State the blood parasite species.
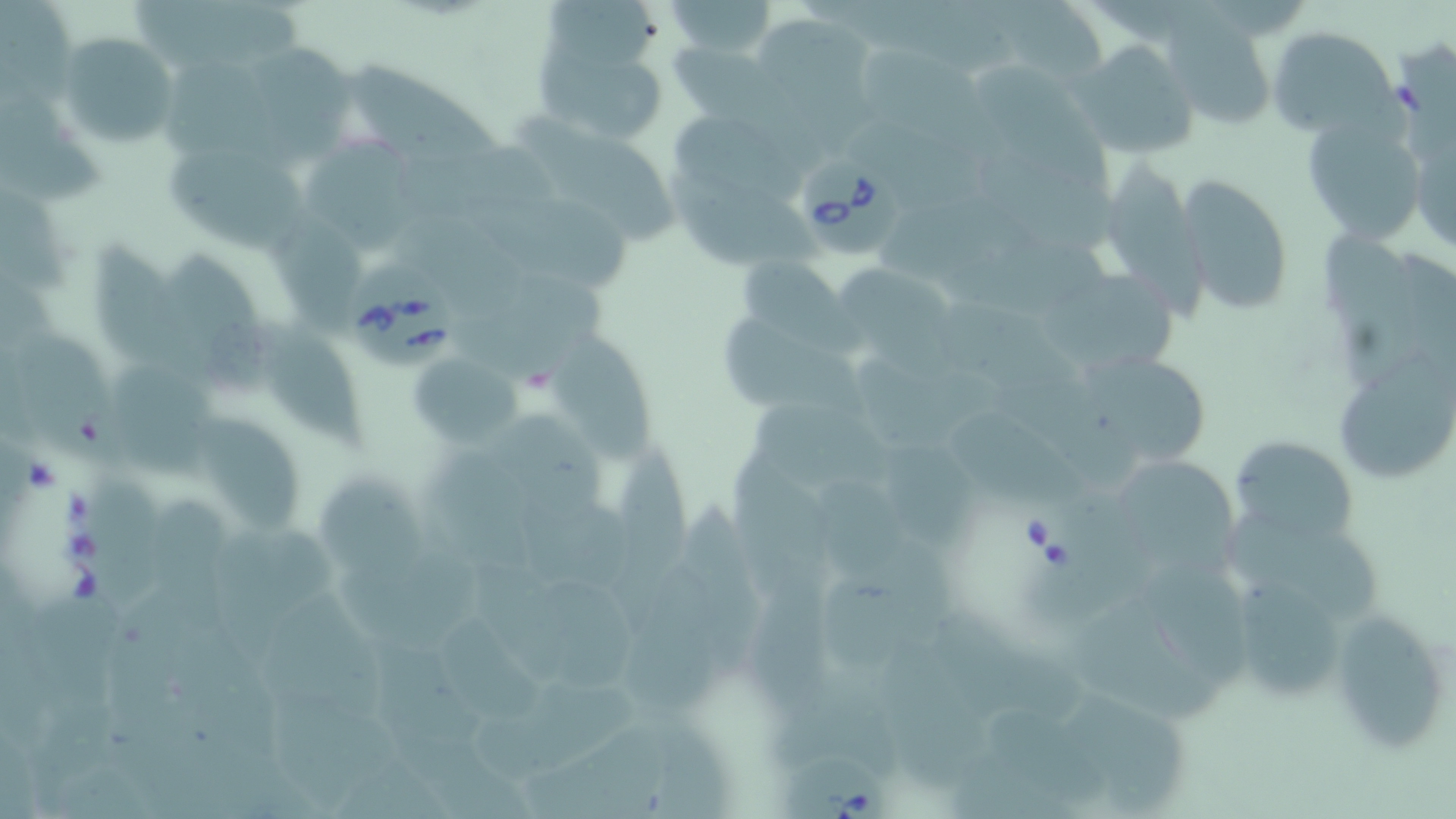

Babesia divergens.

Summary:
  - Coordinate format: approximate bounding boxes as (x1,y1)-(x2,y2) corner pairs in pixels
  - Babesia divergens-infected red blood cell locations: (794,152)-(906,262), (343,260)-(459,365), (1014,489)-(1144,628), (776,746)-(896,819)
  - Uninfected red blood cell locations: (2,0)-(79,103), (133,0)-(302,70), (545,0)-(653,71), (661,0)-(778,59), (1158,12)-(1280,128), (762,15)-(877,149), (1268,27)-(1398,137), (57,33)-(180,147), (853,38)-(1015,162), (535,39)-(668,146), (249,40)-(360,163), (1072,40)-(1200,159), (669,41)-(774,122), (165,53)-(289,163), (344,55)-(495,162), (972,55)-(1111,184), (0,89)-(105,209), (520,106)-(683,252), (1409,109)-(1456,259), (1300,110)-(1427,247), (678,112)-(810,202), (851,130)-(1014,228), (303,131)-(437,248), (394,140)-(560,218), (168,146)-(310,253), (985,151)-(1132,258), (1103,157)-(1206,323), (663,163)-(828,265), (1179,175)-(1295,315), (466,185)-(634,286), (889,207)-(1059,313), (402,208)-(540,304), (1321,228)-(1430,386), (85,234)-(205,372), (171,251)-(278,403), (738,254)-(843,341), (1032,257)-(1186,367), (836,260)-(965,384), (458,272)-(622,385), (934,296)-(1084,390), (261,314)-(368,451), (722,316)-(868,422), (21,326)-(132,470), (552,331)-(654,468), (1343,348)-(1455,485), (1085,351)-(1209,461), (408,354)-(518,449), (113,365)-(220,479), (742,398)-(892,497), (494,409)-(609,528), (960,412)-(1086,503), (193,415)-(298,535), (1231,437)-(1359,547), (613,438)-(696,593), (426,441)-(539,583), (880,443)-(980,552), (1118,457)-(1251,582), (313,471)-(425,579), (84,477)-(176,610), (521,491)-(634,601), (151,499)-(238,631), (679,499)-(773,686), (1223,507)-(1388,627), (218,526)-(330,657), (821,544)-(954,662), (329,548)-(494,647), (1222,564)-(1365,711), (623,565)-(724,714), (747,566)-(844,729), (540,569)-(653,696), (266,596)-(389,722), (1075,600)-(1225,724), (168,602)-(284,760), (1328,604)-(1453,756), (933,606)-(1087,731), (444,615)-(541,722), (374,634)-(485,796), (874,638)-(998,800), (472,681)-(651,784), (256,687)-(407,812), (1073,690)-(1200,812), (519,722)-(673,819)
  - Preparation: thin blood smear
  - Field of view: single
  - Image size: 1456×819 pixels
  - Magnification: 1000x
  - Modality: light microscopy
  - Stain: May-Grünwald-Giemsa